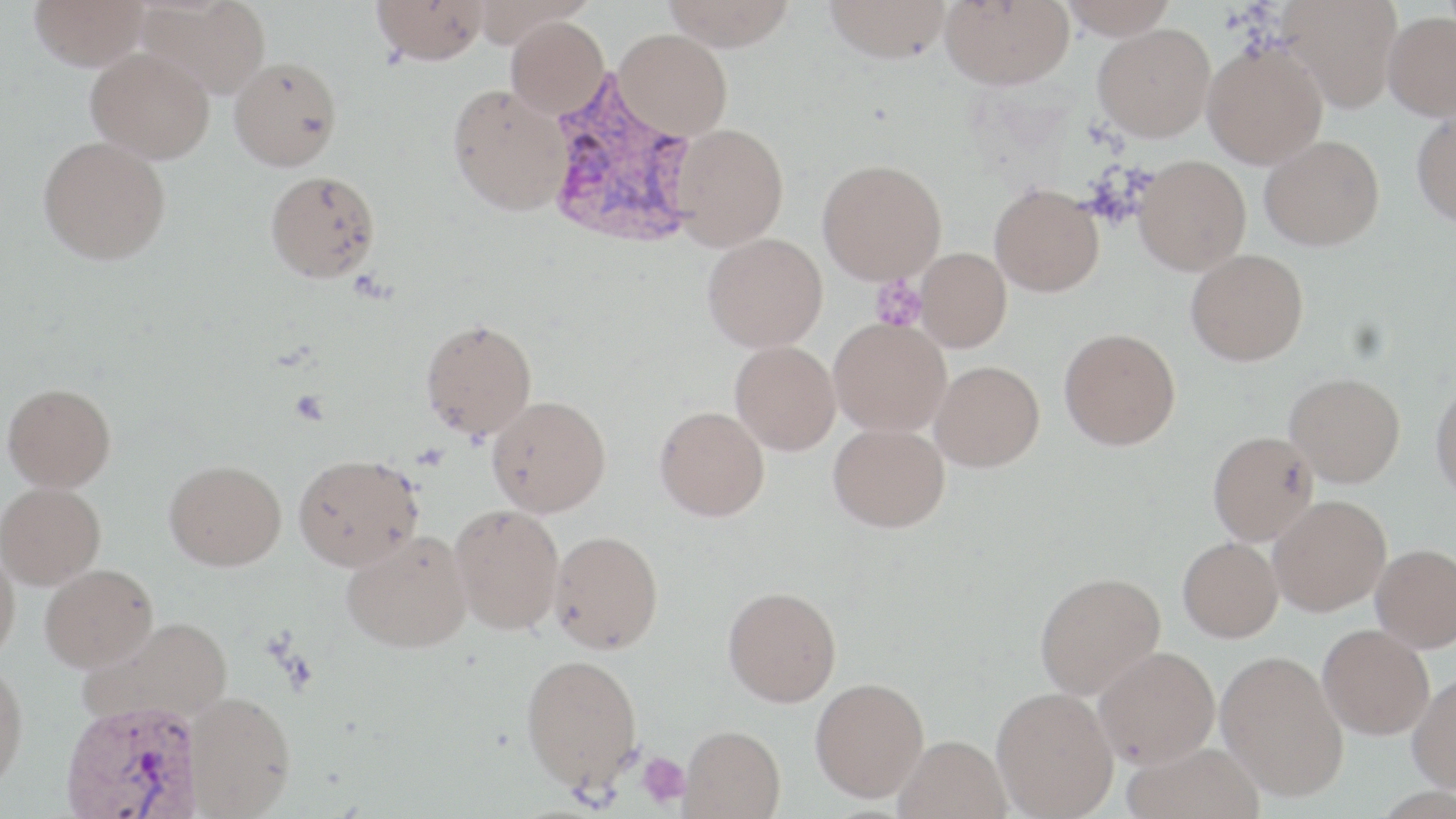
slide-level diagnosis = Plasmodium vivax
uninfected red blood cell locations = approximate bounding boxes as (x1, y1, x2, y2) in pixels: (29, 0, 150, 71), (139, 0, 271, 99), (372, 0, 489, 65), (661, 0, 798, 50), (824, 0, 953, 62), (940, 0, 1074, 89), (1059, 0, 1178, 39), (1281, 0, 1403, 111), (1383, 11, 1456, 120), (505, 16, 609, 119), (1093, 24, 1215, 141), (615, 28, 733, 140), (1202, 41, 1328, 168), (86, 48, 215, 163), (229, 57, 342, 171), (447, 83, 572, 216), (1411, 109, 1456, 226), (671, 123, 789, 250), (38, 135, 171, 264), (1260, 135, 1384, 250), (1134, 155, 1251, 274), (817, 158, 947, 284), (265, 170, 380, 282), (990, 183, 1104, 296), (702, 232, 827, 352), (915, 247, 1011, 352), (1185, 249, 1308, 366), (829, 317, 951, 437), (420, 319, 536, 439), (1059, 328, 1181, 450), (730, 340, 841, 455), (930, 360, 1045, 472), (1284, 372, 1405, 487), (1430, 379, 1456, 503), (3, 383, 117, 490), (487, 395, 611, 516), (655, 405, 770, 521), (828, 423, 950, 532), (1207, 430, 1318, 545), (293, 453, 423, 571), (164, 459, 286, 571), (0, 482, 106, 588), (1268, 495, 1391, 615), (449, 504, 564, 634), (342, 530, 472, 653), (549, 530, 664, 653), (1178, 537, 1283, 643), (1371, 543, 1456, 652), (0, 546, 20, 660), (40, 563, 158, 671), (1034, 571, 1166, 699), (723, 586, 841, 706), (79, 616, 235, 730), (1318, 624, 1435, 739), (1093, 646, 1220, 767), (1216, 649, 1349, 802), (520, 652, 643, 792), (0, 662, 29, 790), (1408, 673, 1456, 794), (810, 677, 928, 801), (992, 687, 1119, 818), (185, 691, 295, 817), (680, 725, 786, 818), (894, 735, 1012, 819), (1123, 742, 1265, 819)
Plasmodium vivax-infected red blood cell locations = approximate bounding boxes as (x1, y1, x2, y2) in pixels: (543, 73, 702, 250), (60, 700, 204, 819)
image size = 1456×819 pixels
field of view = one of a larger specimen
platelet locations = approximate bounding boxes as (x1, y1, x2, y2) in pixels: (870, 275, 925, 331), (636, 751, 691, 808)
modality = optical microscopy
stain = May-Grünwald-Giemsa
preparation = thin blood smear
magnification = 1000x